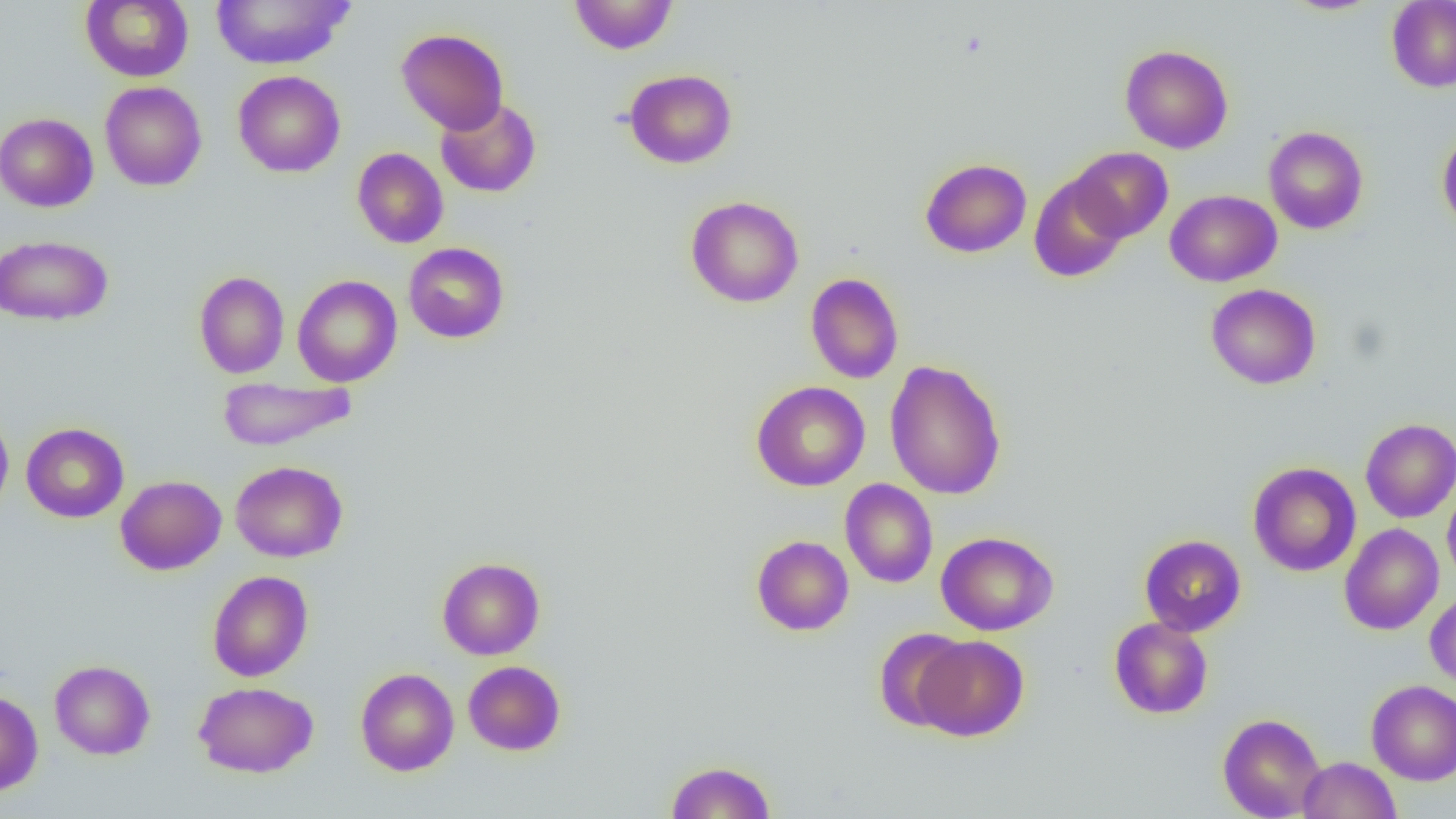

Summary:
  - Coordinate format: approximate bounding boxes as [x1, y1, x2, y2] in pixels
  - Uninfected red blood cell locations: [210, 0, 355, 70], [569, 0, 678, 55], [1281, 0, 1383, 16], [1386, 0, 1456, 92], [81, 1, 193, 82], [396, 28, 509, 135], [1120, 44, 1234, 153], [624, 69, 737, 169], [233, 70, 345, 177], [100, 81, 207, 191], [436, 97, 541, 198], [0, 112, 99, 212], [1263, 126, 1369, 234], [1437, 128, 1456, 234], [352, 147, 448, 248], [1069, 147, 1173, 243], [920, 159, 1031, 257], [1029, 173, 1129, 283], [1165, 190, 1282, 286], [686, 195, 804, 307], [0, 235, 113, 325], [403, 242, 509, 344], [194, 271, 289, 379], [805, 273, 904, 383], [292, 275, 402, 387], [1206, 284, 1321, 390], [885, 359, 1006, 499], [217, 377, 357, 451], [751, 381, 870, 491], [0, 410, 14, 520], [1355, 418, 1449, 634], [1360, 418, 1456, 523], [21, 422, 129, 523], [230, 460, 347, 562], [1248, 462, 1361, 576], [115, 475, 227, 575], [840, 478, 938, 588], [1442, 481, 1456, 586], [1340, 523, 1444, 635], [936, 531, 1058, 636], [1139, 534, 1246, 636], [751, 535, 853, 636], [436, 557, 545, 660], [207, 570, 313, 681], [1425, 590, 1456, 689], [1109, 617, 1213, 719], [874, 628, 970, 732], [913, 635, 1029, 741], [49, 660, 155, 759], [463, 660, 565, 755], [355, 667, 459, 776], [1366, 679, 1456, 785], [193, 681, 318, 778], [0, 690, 43, 795], [1217, 713, 1326, 818], [1298, 756, 1401, 819], [665, 760, 776, 819]
  - Slide-level diagnosis: no evidence of blood parasites
  - Modality: optical microscopy
  - Image size: 1456×819 pixels
  - Preparation: thin blood film
  - Field of view: one of a larger specimen
  - Magnification: 1000x